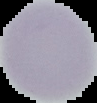
{
  "image_type": "segmented cell region with the area outside set to black",
  "malaria_status": "uninfected",
  "preparation": "thin blood film",
  "image_size": "97×103 pixels"
}